Name the parasite shown.
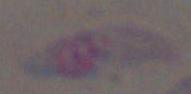
This is Toxoplasma gondii.

Micrograph. 1000x magnification.